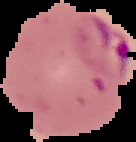

From a thin blood smear. Result: malaria parasites detected. Image is 136×142 pixels. Segmented cell region on a black background.